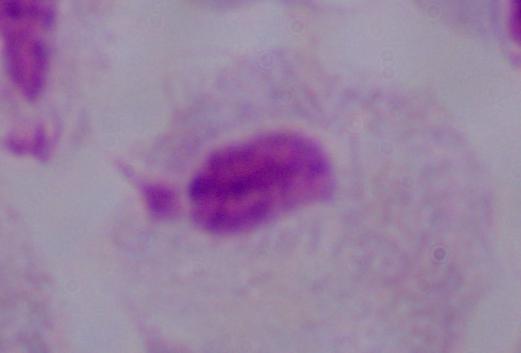

Summary:
  - Identification: trichomonad
  - Magnification: 1000x
  - Modality: photomicrograph